Report the malaria status of this cell.
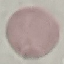
Uninfected.

Acquired by smartphone through the microscope eyepiece. Giemsa stain. Thin blood smear. Cell patch, automatically extracted from a larger field of view and resized to 64 × 64 pixels.